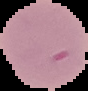

Summary:
  - Preparation: thin blood film
  - Image type: cell region segmented out of the field of view; surrounding area masked to black
  - Image size: 88×91 pixels
  - Malaria status: uninfected